Assess this cell for malaria.
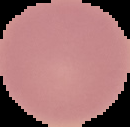

It is uninfected.

Image is 130×127 pixels. The area outside the segmented cell region is set to black. From a thin blood film.